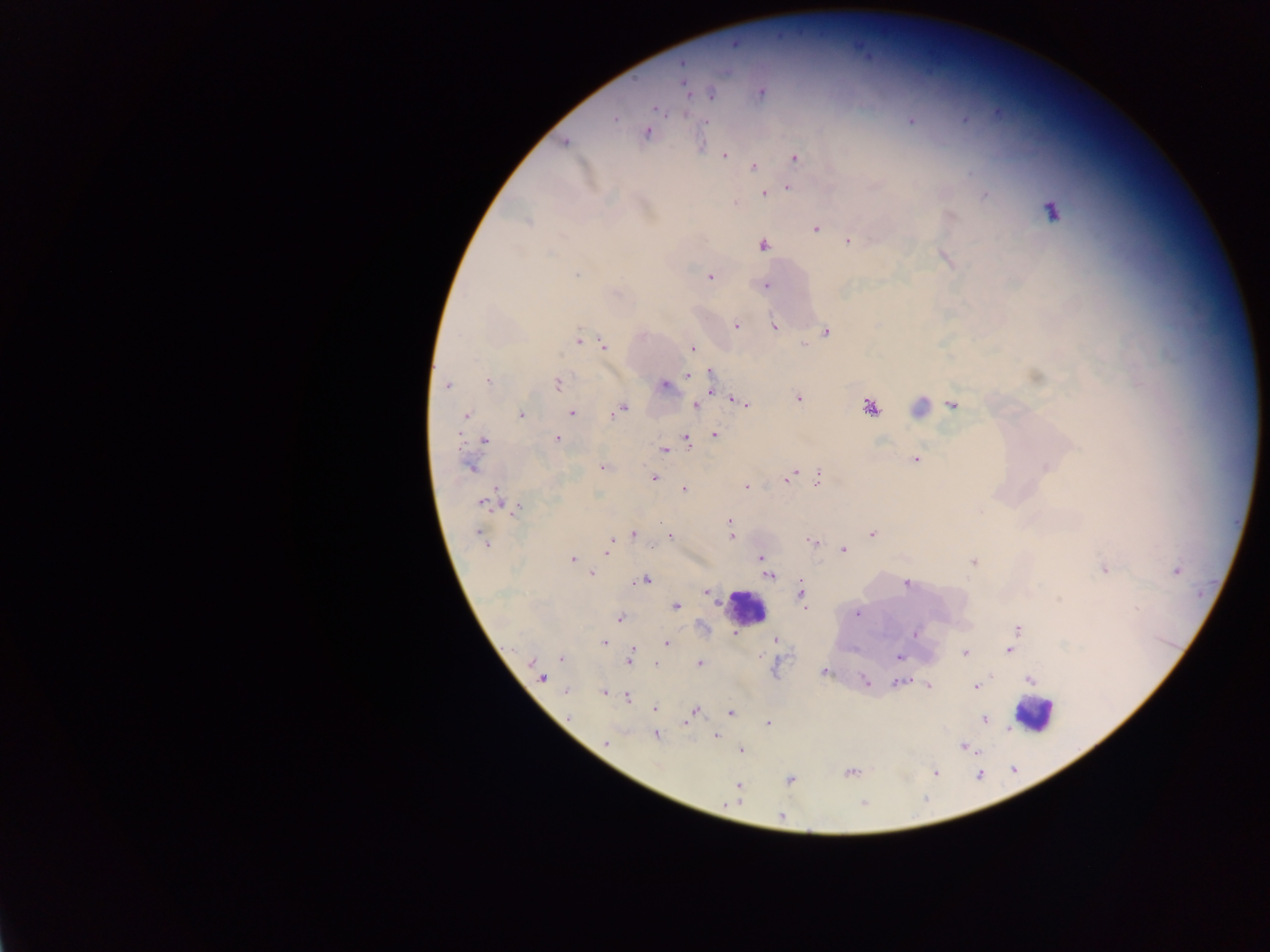
Approximate centers as (x, y) in pixels.
Summary:
  - Leukocyte locations: (742, 602), (1035, 707)
  - Plasmodium parasite locations: (683, 65), (686, 85), (760, 93), (711, 94), (654, 108), (996, 113), (684, 116), (615, 119), (963, 119), (910, 121), (705, 122), (647, 132), (565, 142), (725, 154), (797, 158), (753, 167), (788, 186), (766, 194), (985, 196), (527, 221), (816, 229), (848, 241), (764, 245), (575, 274), (709, 277), (766, 285), (736, 326), (773, 326), (828, 332), (579, 340), (803, 344), (605, 345), (692, 347), (1034, 376), (687, 377), (487, 381), (558, 384), (446, 385), (663, 386), (712, 390), (734, 399), (798, 399), (748, 404), (953, 405), (697, 406), (923, 406), (624, 408), (868, 408), (521, 414), (572, 414), (466, 416), (715, 433), (558, 438), (484, 440), (686, 441), (665, 450), (915, 459), (601, 467), (471, 468), (1045, 468), (795, 472), (653, 478), (787, 479), (818, 479), (747, 487), (684, 488), (496, 491), (481, 502), (519, 505), (504, 507), (517, 509), (729, 522), (480, 532), (733, 532), (633, 534), (871, 534), (671, 535), (732, 536), (610, 540), (811, 542), (609, 548), (844, 550), (607, 552), (760, 558), (574, 560), (973, 561), (1106, 570), (1177, 570), (591, 574), (769, 577), (647, 581), (906, 584), (706, 592), (798, 593), (1058, 598), (718, 605), (676, 607), (804, 607), (1137, 610), (858, 613), (619, 619), (1018, 628), (732, 632), (915, 633), (775, 640), (605, 643), (667, 644), (1010, 649), (633, 650), (964, 654), (899, 657), (530, 661), (629, 662), (700, 662), (655, 663), (824, 671), (544, 678), (1030, 680), (865, 681), (896, 682), (910, 683), (929, 685), (976, 687), (566, 691), (604, 693), (628, 696), (1052, 704), (654, 708), (695, 711), (731, 712), (987, 718), (686, 725), (1007, 729), (716, 735), (655, 736), (606, 742), (963, 746), (982, 749), (740, 751), (848, 773), (781, 818)
  - Preparation: thick blood smear
  - Field of view: single
  - Country: Ghana
  - Image size: 1270×952 pixels
  - Capture: mobile-phone photograph through a microscope